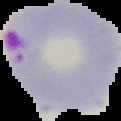 Image is 121×121 pixels. Malaria status: parasitized. Segmented cell region on a black background. From a thin blood film.